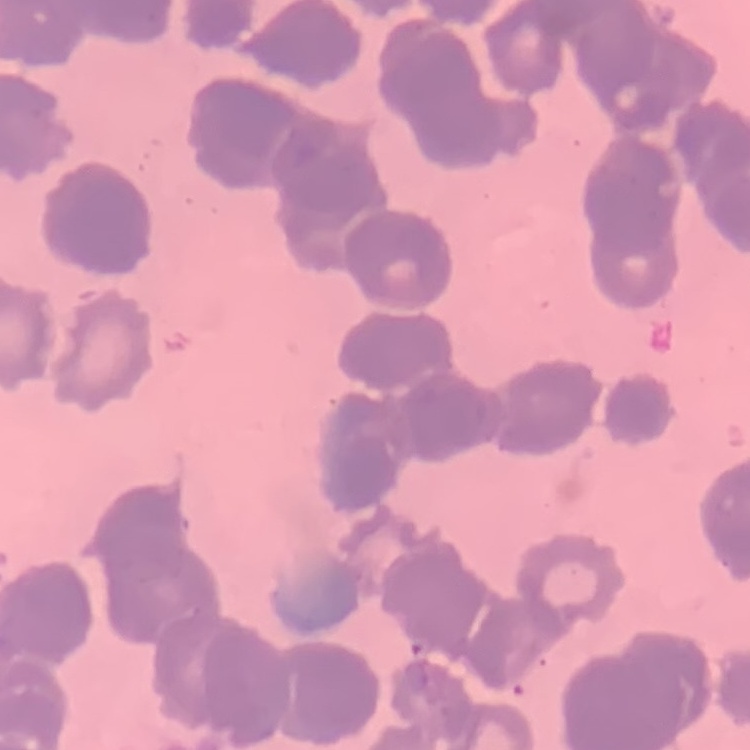

Summary:
  - Red blood cell morphology: rouleaux formation
  - Image type: one tile cut from a larger photomicrograph
  - Preparation: thin blood smear
  - Stain: Field's or Giemsa